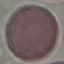
Malaria status: uninfected. Automatically extracted cell patch, resized to 64 × 64 pixels. Giemsa stain. Acquired by smartphone through the microscope eyepiece. Thin blood smear.